Name the parasite shown.
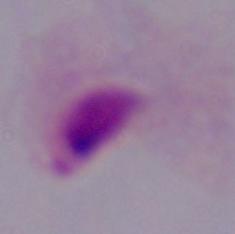
This is a trichomonad.

Summary:
  - Magnification: 1000x
  - Modality: micrograph